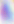
identification = Toxoplasma gondii
modality = photomicrograph
magnification = 400x